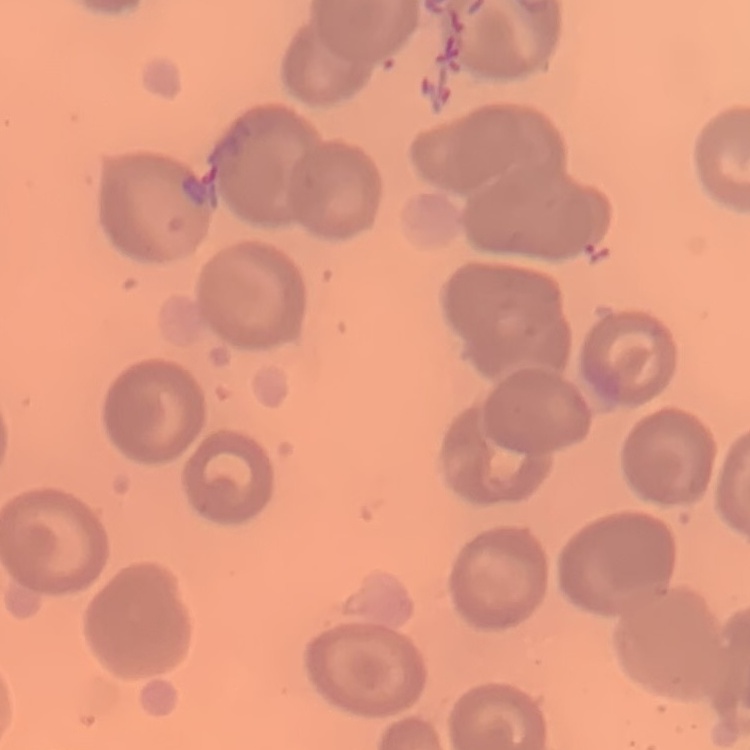
red blood cell morphology = no rouleaux formation
preparation = thin peripheral smear
image type = square crop of a larger photomicrograph
stain = Field's or Giemsa